Describe the morphology of the red blood cells.
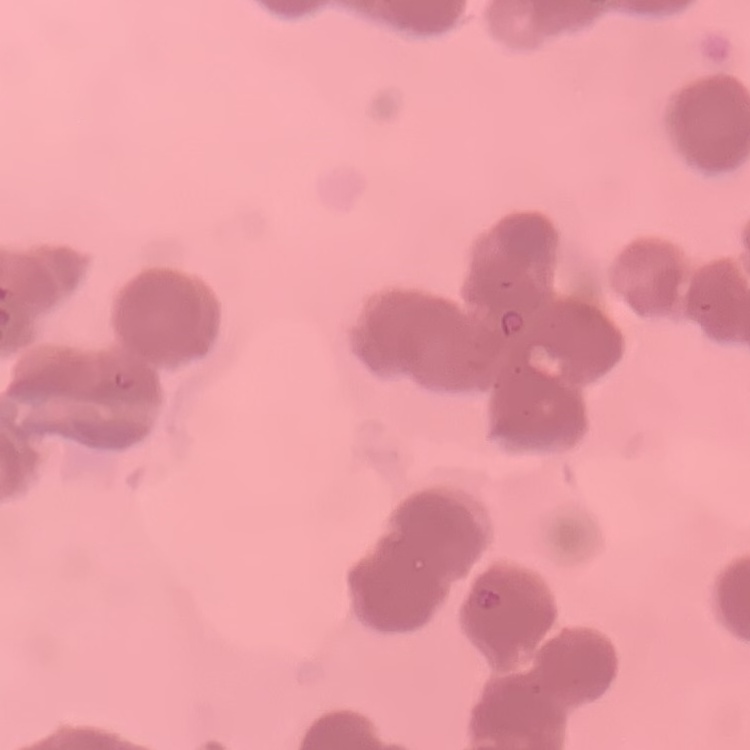

Rouleaux formation.

Stained with either Field's or Giemsa. Thin blood film. One tile cut from a larger photomicrograph.